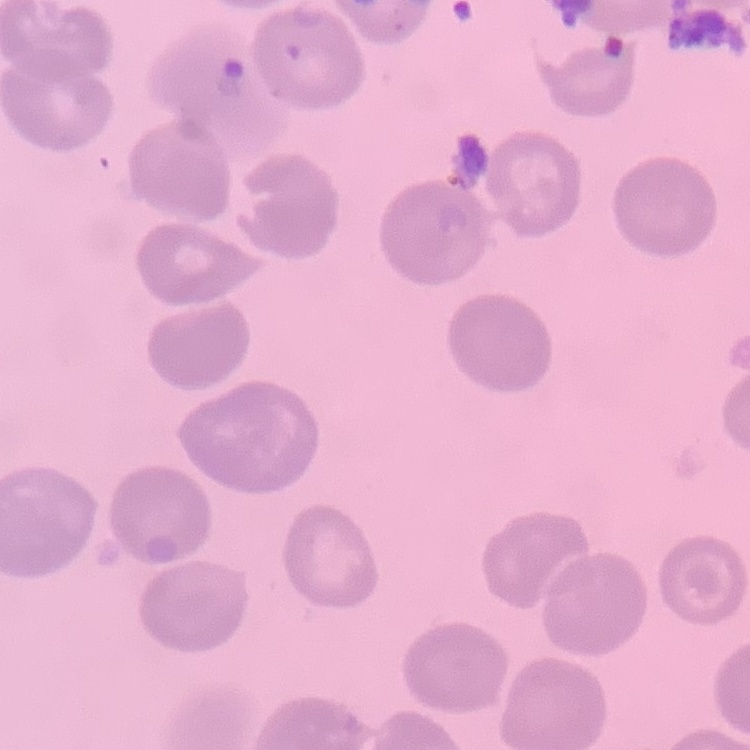

red blood cell morphology = no rouleaux formation
image type = one tile cut from a larger photomicrograph
stain = Field's or Giemsa
preparation = thin peripheral smear